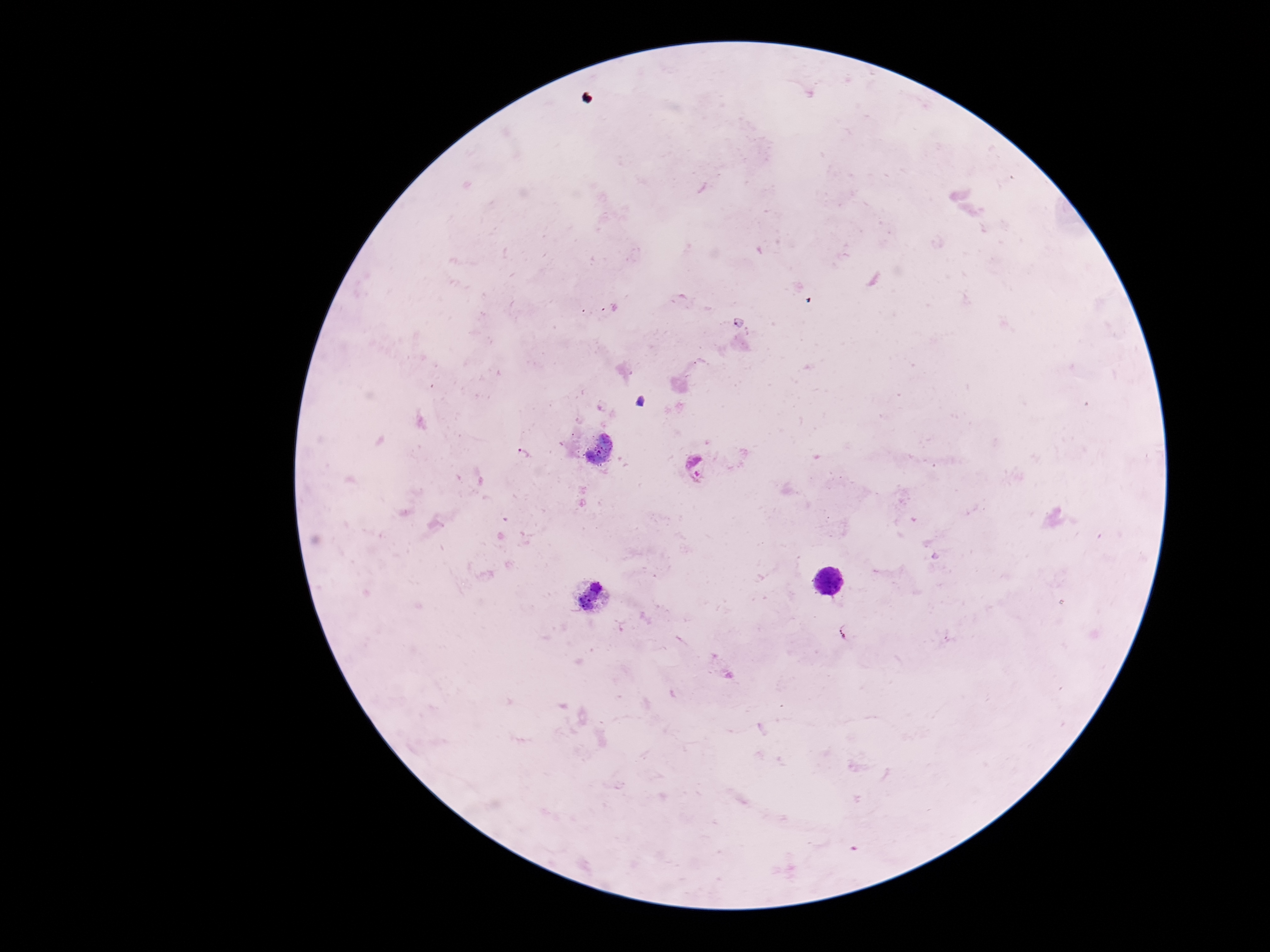
Approximate centers as {x, y} in pixels.
Summary:
  - Plasmodium parasite locations: {523, 454}, {695, 468}
  - Patient malaria status: positive
  - Capture: smartphone camera through the microscope eyepiece
  - Field of view: single
  - Image size: 1270×952 pixels
  - Stain: Giemsa
  - Preparation: thick blood film
  - Magnification: 100x